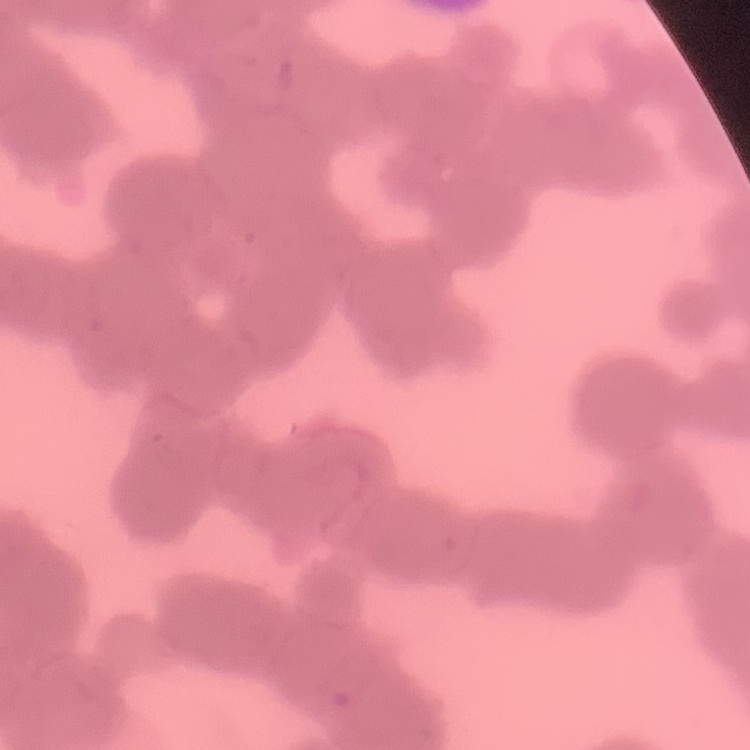

Summary:
  - Erythrocyte morphology: rouleaux formation
  - Preparation: thin peripheral smear
  - Image type: one tile cut from a larger photomicrograph
  - Stain: Field's or Giemsa